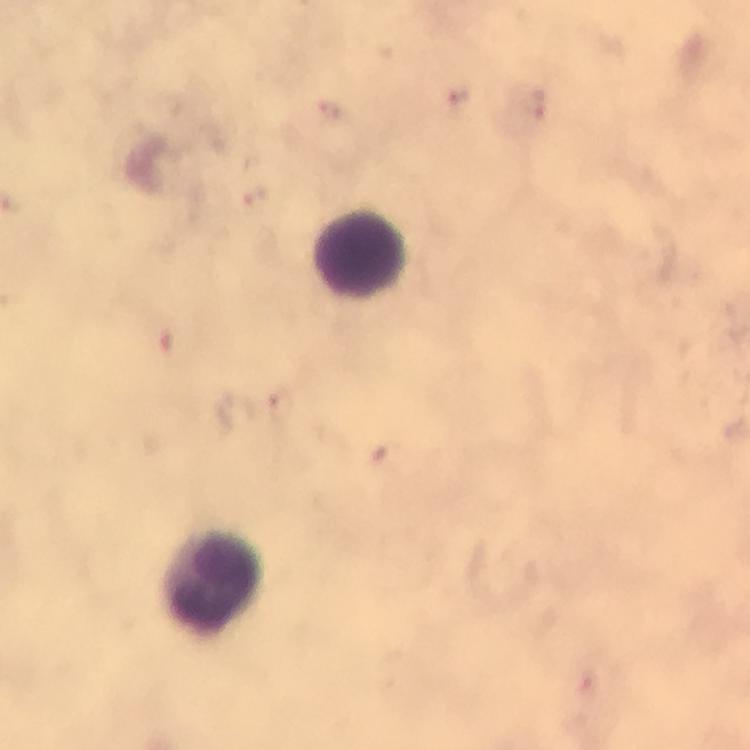

Approximate centers as {x, y} in pixels. Leukocyte locations: {360, 253}, {212, 581}. Thick blood film. Plasmodium parasites: none detected. At 100x magnification. From a diagnostic examination for malaria. Image is 750×750 pixels. Immersion oil was used. Photographed through the microscope with a smartphone camera. Cropped region of a single field of view. Giemsa stain.